Classify this cell by malaria status.
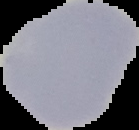
It is uninfected.

image type = segmented cell region on a black background
preparation = thin blood smear
image size = 139×130 pixels